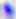 Micrograph. Toxoplasma gondii is shown. 400x magnification.